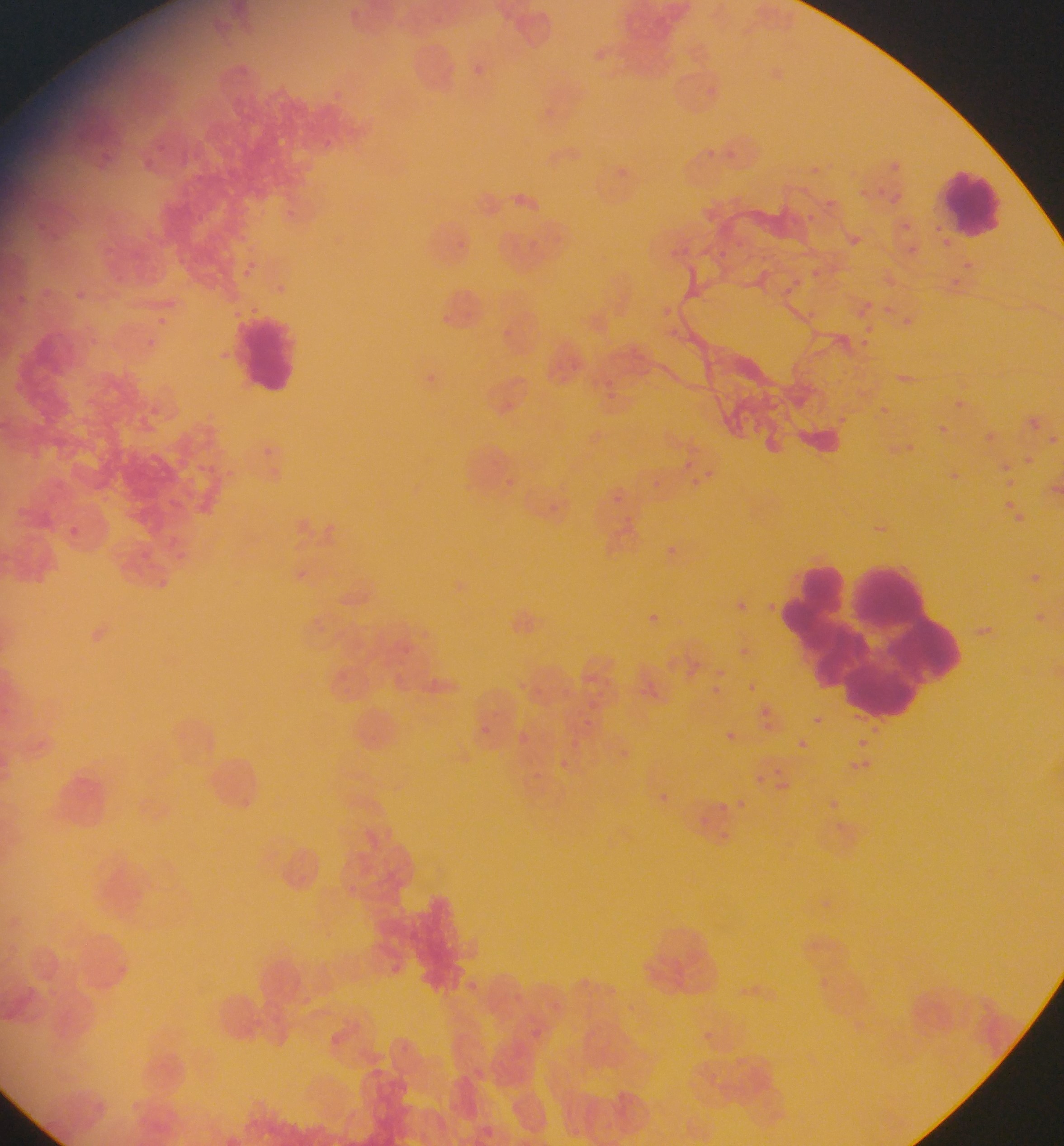
{
  "preparation": "thin blood film",
  "capture": "mobile-phone photograph through a microscope",
  "field_of_view": "single",
  "leukocyte_locations": "approximate bounding boxes as left top right bottom in pixels: 237 313 302 393; 786 555 976 722",
  "object_labeled_both_malaria_parasite_and_leukocyte_by_the_source": "approximate bounding boxes as left top right bottom in pixels: 937 172 1005 247",
  "image_size": "1064×1146 pixels",
  "country": "Ghana",
  "malaria_parasite_locations": "approximate bounding boxes as left top right bottom in pixels: 475 64 484 73; 728 147 750 169; 889 159 911 169; 811 162 826 174; 869 182 879 193; 897 191 908 203; 824 197 845 209; 898 205 915 235; 801 209 820 223; 849 235 883 255; 903 241 924 258; 960 258 974 271; 812 260 824 272; 949 279 971 298; 859 297 876 315; 153 314 170 330; 898 314 915 330; 142 336 158 352; 856 339 878 351; 427 369 439 384; 951 396 967 411; 883 402 903 424; 832 412 870 437; 934 422 950 437; 980 428 997 445; 1046 433 1063 448; 904 442 919 464; 669 454 691 469; 1008 459 1025 482; 706 464 730 481; 945 468 962 485; 699 477 713 492; 1002 498 1015 513; 1002 500 1025 523; 661 541 681 561; 1031 562 1039 579; 764 597 786 615; 725 598 743 613; 646 609 658 621; 740 644 752 660; 709 664 726 676; 641 677 654 694; 702 680 721 697; 746 680 759 695; 810 713 825 727; 582 716 593 729; 472 724 501 746; 720 728 739 746; 513 731 534 745; 794 737 809 751; 856 737 869 749; 561 740 583 748; 613 741 633 765; 849 756 872 775; 559 759 566 775; 755 770 767 785; 656 793 670 804; 821 796 842 816; 731 797 745 818; 712 799 728 818; 694 813 705 826; 706 830 729 843"
}